Report the malaria status of this cell.
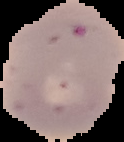
Parasitized.

preparation = thin blood film
image type = segmented cell region on a black background
image size = 124×142 pixels